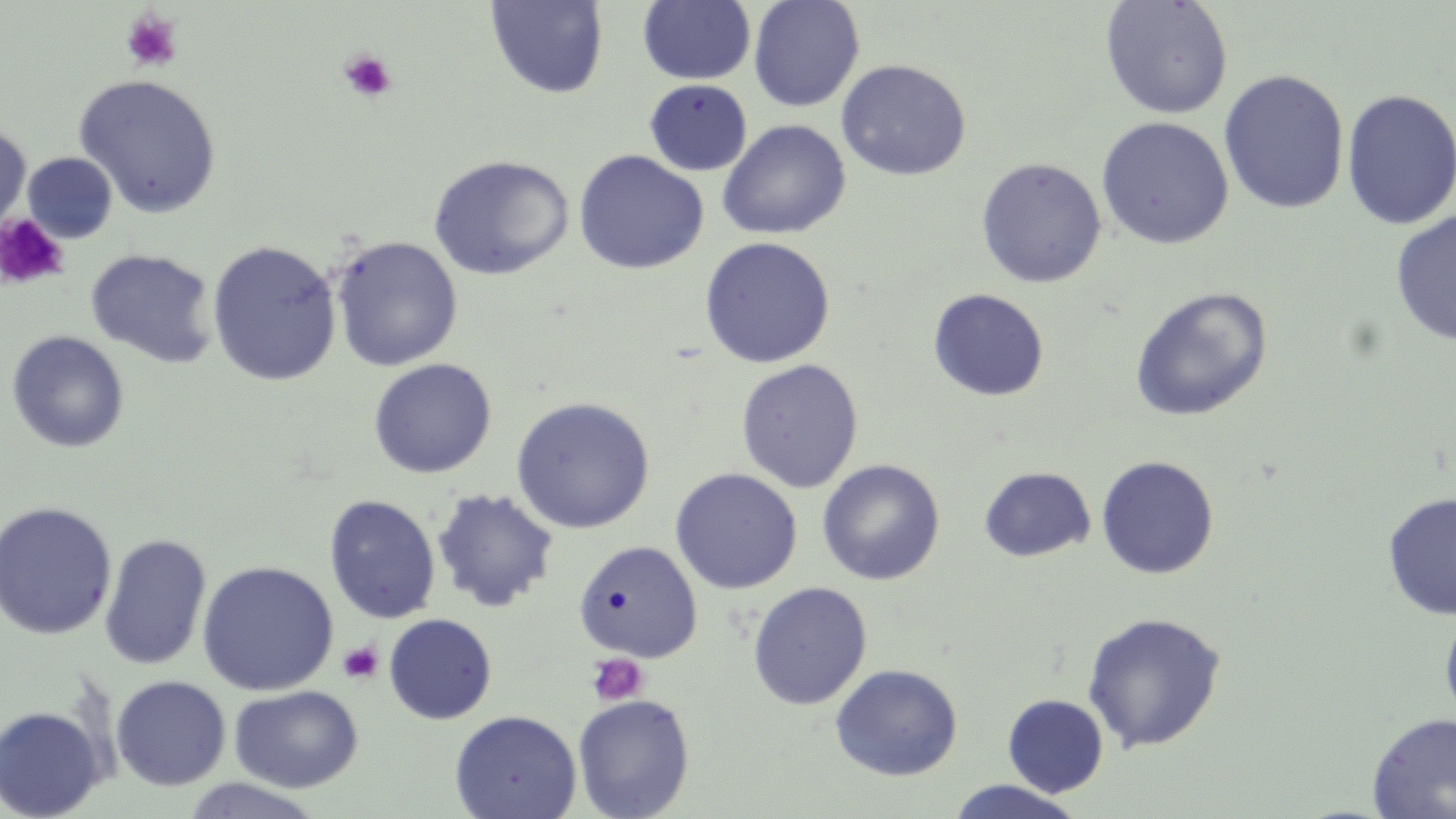

Approximate bounding boxes as (x1, y1, x2, y2) in pixels. Uninfected red blood cell locations: (637, 0, 756, 85), (747, 0, 865, 112), (1100, 0, 1234, 119), (485, 1, 608, 99), (836, 59, 972, 181), (1218, 69, 1350, 215), (73, 74, 222, 218), (644, 79, 753, 176), (1341, 89, 1456, 231), (1096, 117, 1234, 249), (717, 120, 851, 240), (0, 124, 32, 235), (573, 149, 708, 275), (22, 152, 118, 244), (427, 154, 575, 281), (975, 157, 1107, 288), (1390, 209, 1456, 347), (330, 236, 464, 372), (698, 236, 836, 369), (206, 241, 342, 386), (85, 248, 219, 368), (1129, 286, 1273, 422), (927, 288, 1050, 401), (5, 331, 130, 453), (367, 358, 497, 479), (735, 358, 864, 493), (510, 396, 656, 534), (1096, 456, 1219, 579), (817, 459, 945, 585), (978, 466, 1096, 563), (670, 468, 802, 594), (431, 488, 559, 613), (1381, 492, 1456, 620), (323, 495, 441, 624), (0, 501, 117, 640), (99, 533, 211, 671), (574, 541, 703, 663), (196, 561, 338, 696), (747, 582, 872, 711), (1439, 604, 1456, 728), (1080, 611, 1227, 753), (383, 613, 498, 725), (829, 664, 963, 781), (110, 675, 231, 791), (229, 685, 363, 793), (572, 694, 695, 819), (1002, 694, 1108, 797), (0, 704, 108, 819), (449, 710, 582, 819), (1366, 712, 1456, 818), (178, 778, 328, 818), (945, 779, 1086, 818). Platelet locations: (120, 9, 182, 72), (337, 49, 397, 102), (0, 213, 70, 290), (337, 641, 384, 684), (586, 653, 649, 707). Slide-level diagnosis: no evidence of blood parasites. Captured at 1000x magnification. Thin blood film. Image is 1456×819 pixels. May-Grünwald-Giemsa stain. One field of a larger specimen. Light microscopy.